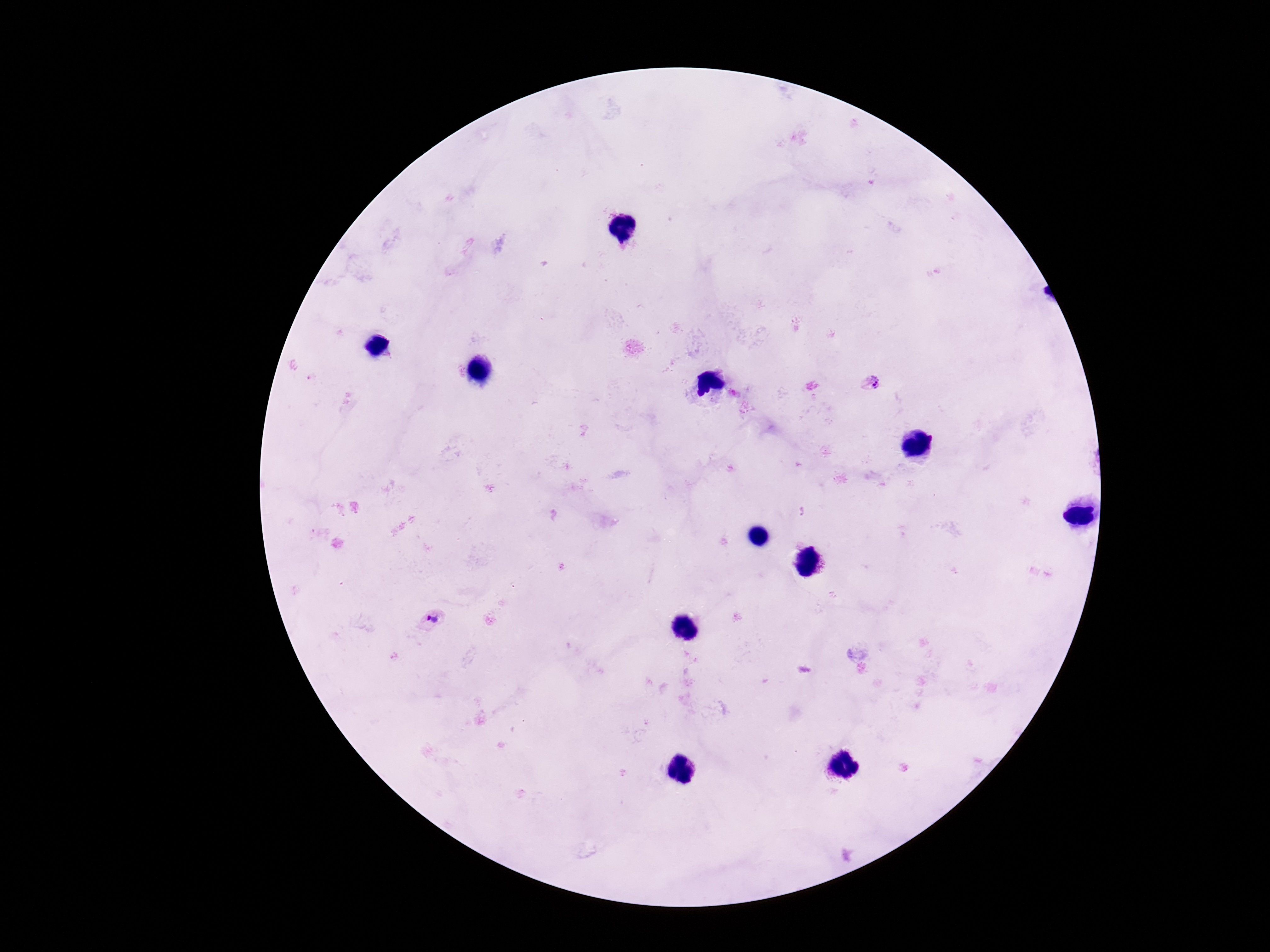
Approximate centers as [x, y] in pixels. Plasmodium parasite locations: [872, 383], [433, 618]. Image is 1270×952 pixels. Thick blood smear. Photographed through the microscope eyepiece with a smartphone camera. Single field of view. Patient malaria status: positive. Giemsa stain. 100x magnification.